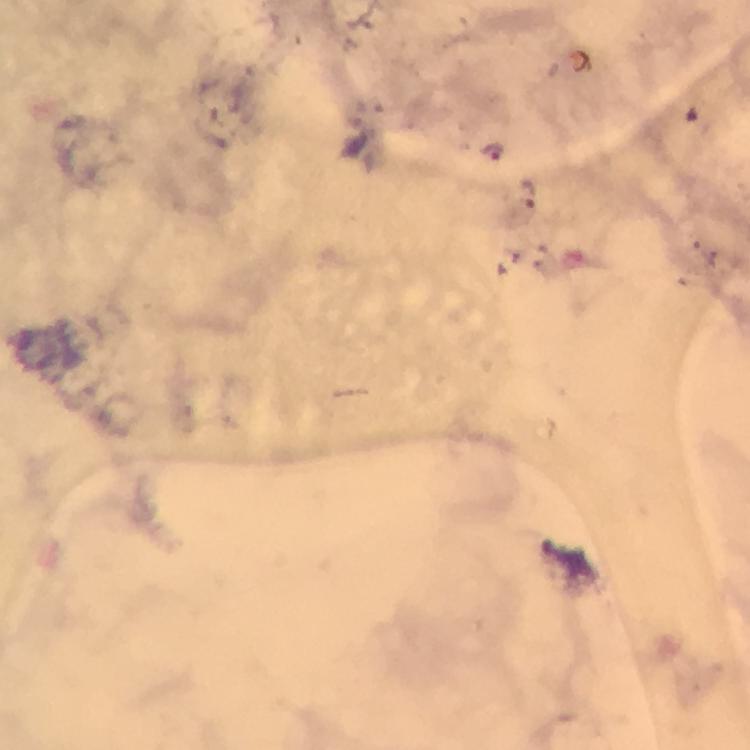
{
  "immersion_oil": "applied",
  "cropped_from": "a single field of view",
  "plasmodium_parasite_locations": "approximate object centers, in pixels from the top-left corner: (x=491, y=150), (x=530, y=193)",
  "stain": "Giemsa",
  "context": "from a malaria diagnostic workup",
  "capture": "smartphone camera through the microscope",
  "magnification": "100x",
  "preparation": "thick blood smear",
  "image_size": "750×750 pixels"
}